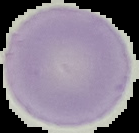

Summary:
  - Preparation: thin blood smear
  - Image type: segmented cell region with the area outside set to black
  - Malaria status: uninfected
  - Image size: 139×133 pixels